Classify this cell by malaria status.
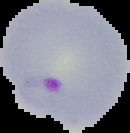
Parasitized.

From a thin blood smear. Image is 130×133 pixels. Cell region segmented out of the field of view; the surrounding area is masked to black.